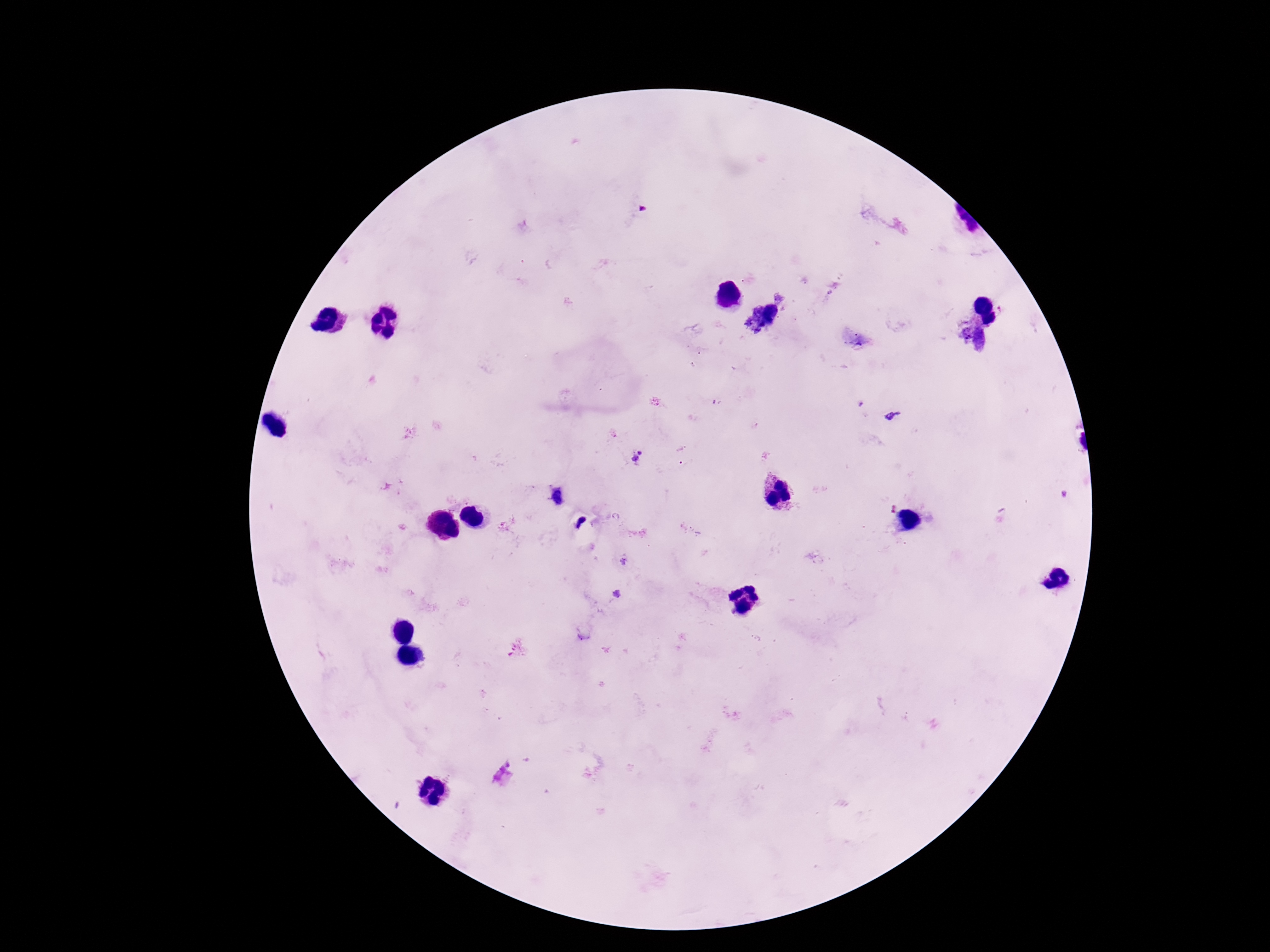

preparation: thick blood film
patient_malaria_status: positive
plasmodium_parasite_locations: 'approximate object centers, in pixels from the top-left corner: (x=893, y=416), (x=636, y=458)'
capture: smartphone camera through the microscope eyepiece
magnification: 100x
image_size: 1270×952 pixels
stain: Giemsa
field_of_view: one from this slide